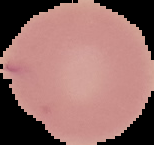

Summary:
  - Preparation: thin blood film
  - Image size: 154×145 pixels
  - Malaria status: uninfected
  - Image type: segmented cell region on a black background